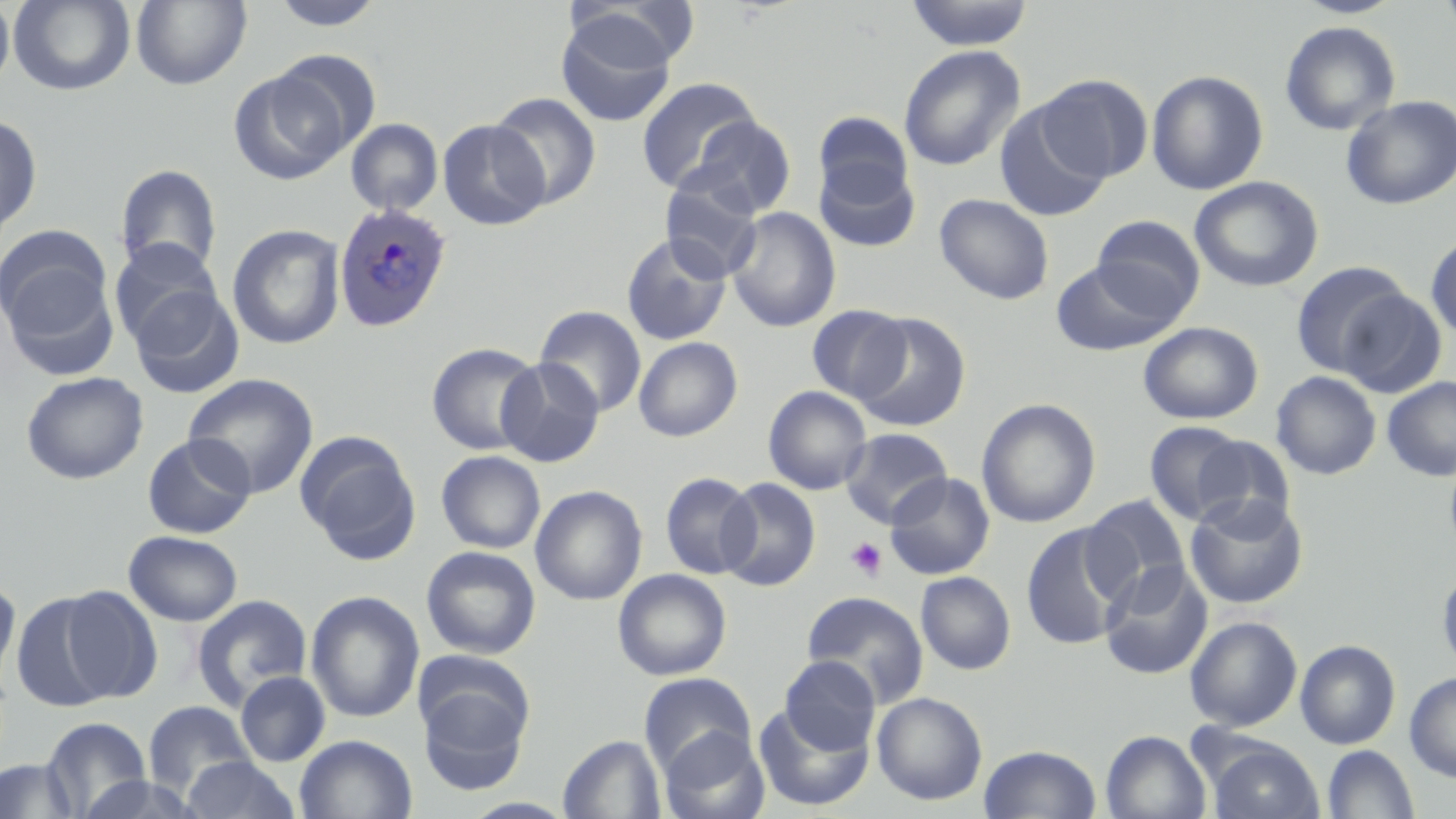

Approximate bounding boxes as named x1/y1/x2/y2 corners in pixels. Plasmodium ovale-infected red blood cell locations: (x1=333, y1=201, x2=453, y2=333). Platelet locations: (x1=845, y1=537, x2=888, y2=582). Uninfected red blood cell locations: (x1=8, y1=0, x2=136, y2=96), (x1=269, y1=0, x2=387, y2=31), (x1=905, y1=0, x2=1035, y2=50), (x1=1294, y1=0, x2=1405, y2=19), (x1=1438, y1=0, x2=1456, y2=41), (x1=0, y1=1, x2=15, y2=97), (x1=131, y1=1, x2=251, y2=89), (x1=563, y1=3, x2=695, y2=75), (x1=556, y1=13, x2=676, y2=127), (x1=1279, y1=20, x2=1401, y2=136), (x1=898, y1=44, x2=1026, y2=171), (x1=272, y1=49, x2=382, y2=154), (x1=228, y1=69, x2=351, y2=184), (x1=1146, y1=69, x2=1269, y2=196), (x1=1037, y1=74, x2=1152, y2=182), (x1=636, y1=77, x2=762, y2=194), (x1=489, y1=92, x2=602, y2=209), (x1=1341, y1=95, x2=1456, y2=209), (x1=994, y1=101, x2=1111, y2=222), (x1=812, y1=111, x2=916, y2=207), (x1=0, y1=114, x2=42, y2=239), (x1=685, y1=115, x2=797, y2=218), (x1=345, y1=118, x2=443, y2=216), (x1=437, y1=119, x2=551, y2=230), (x1=814, y1=159, x2=921, y2=252), (x1=115, y1=164, x2=222, y2=276), (x1=659, y1=175, x2=765, y2=281), (x1=1189, y1=176, x2=1324, y2=292), (x1=935, y1=193, x2=1054, y2=304), (x1=725, y1=206, x2=841, y2=332), (x1=1091, y1=215, x2=1205, y2=317), (x1=0, y1=224, x2=112, y2=333), (x1=226, y1=224, x2=347, y2=350), (x1=1425, y1=231, x2=1456, y2=343), (x1=621, y1=232, x2=732, y2=346), (x1=108, y1=238, x2=224, y2=347), (x1=3, y1=258, x2=120, y2=379), (x1=1052, y1=258, x2=1182, y2=357), (x1=1291, y1=261, x2=1413, y2=378), (x1=129, y1=285, x2=244, y2=399), (x1=1334, y1=288, x2=1447, y2=398), (x1=533, y1=305, x2=647, y2=417), (x1=806, y1=305, x2=911, y2=403), (x1=851, y1=313, x2=970, y2=433), (x1=1138, y1=322, x2=1263, y2=424), (x1=633, y1=336, x2=743, y2=441), (x1=426, y1=342, x2=543, y2=455), (x1=496, y1=357, x2=604, y2=467), (x1=21, y1=371, x2=149, y2=484), (x1=1271, y1=371, x2=1381, y2=479), (x1=183, y1=372, x2=319, y2=499), (x1=1382, y1=377, x2=1456, y2=481), (x1=763, y1=386, x2=872, y2=495), (x1=976, y1=398, x2=1100, y2=528), (x1=1144, y1=421, x2=1250, y2=525), (x1=840, y1=428, x2=952, y2=527), (x1=295, y1=432, x2=421, y2=564), (x1=142, y1=434, x2=256, y2=539), (x1=1191, y1=435, x2=1296, y2=532), (x1=1444, y1=449, x2=1456, y2=563), (x1=436, y1=450, x2=545, y2=554), (x1=660, y1=471, x2=760, y2=579), (x1=885, y1=472, x2=995, y2=580), (x1=717, y1=477, x2=821, y2=592), (x1=530, y1=485, x2=648, y2=606), (x1=1082, y1=494, x2=1191, y2=603), (x1=1184, y1=494, x2=1309, y2=609), (x1=1022, y1=523, x2=1130, y2=651), (x1=124, y1=531, x2=242, y2=626), (x1=421, y1=545, x2=541, y2=659), (x1=1099, y1=560, x2=1213, y2=680), (x1=1437, y1=565, x2=1456, y2=676), (x1=612, y1=568, x2=732, y2=681), (x1=916, y1=572, x2=1016, y2=674), (x1=0, y1=581, x2=21, y2=682), (x1=56, y1=585, x2=162, y2=703), (x1=304, y1=590, x2=426, y2=723), (x1=11, y1=591, x2=119, y2=712), (x1=801, y1=591, x2=929, y2=707), (x1=192, y1=594, x2=313, y2=709), (x1=1185, y1=616, x2=1303, y2=731), (x1=1295, y1=639, x2=1401, y2=749), (x1=779, y1=656, x2=880, y2=755), (x1=235, y1=671, x2=331, y2=767), (x1=416, y1=672, x2=534, y2=795), (x1=639, y1=672, x2=756, y2=775), (x1=1404, y1=672, x2=1456, y2=781), (x1=872, y1=691, x2=988, y2=805), (x1=142, y1=701, x2=256, y2=795), (x1=753, y1=703, x2=873, y2=811), (x1=42, y1=717, x2=151, y2=816), (x1=659, y1=728, x2=769, y2=819), (x1=1101, y1=730, x2=1212, y2=819), (x1=294, y1=734, x2=417, y2=818), (x1=558, y1=734, x2=667, y2=819), (x1=1206, y1=740, x2=1325, y2=819), (x1=979, y1=744, x2=1102, y2=818), (x1=1322, y1=745, x2=1419, y2=819), (x1=181, y1=756, x2=299, y2=818), (x1=0, y1=758, x2=80, y2=819), (x1=75, y1=774, x2=206, y2=818). Slide-level diagnosis: Plasmodium ovale. One field of a larger specimen. Optical microscopy. Image is 1456×819 pixels. May-Grünwald-Giemsa-stained preparation. 1000x magnification. Thin blood smear.